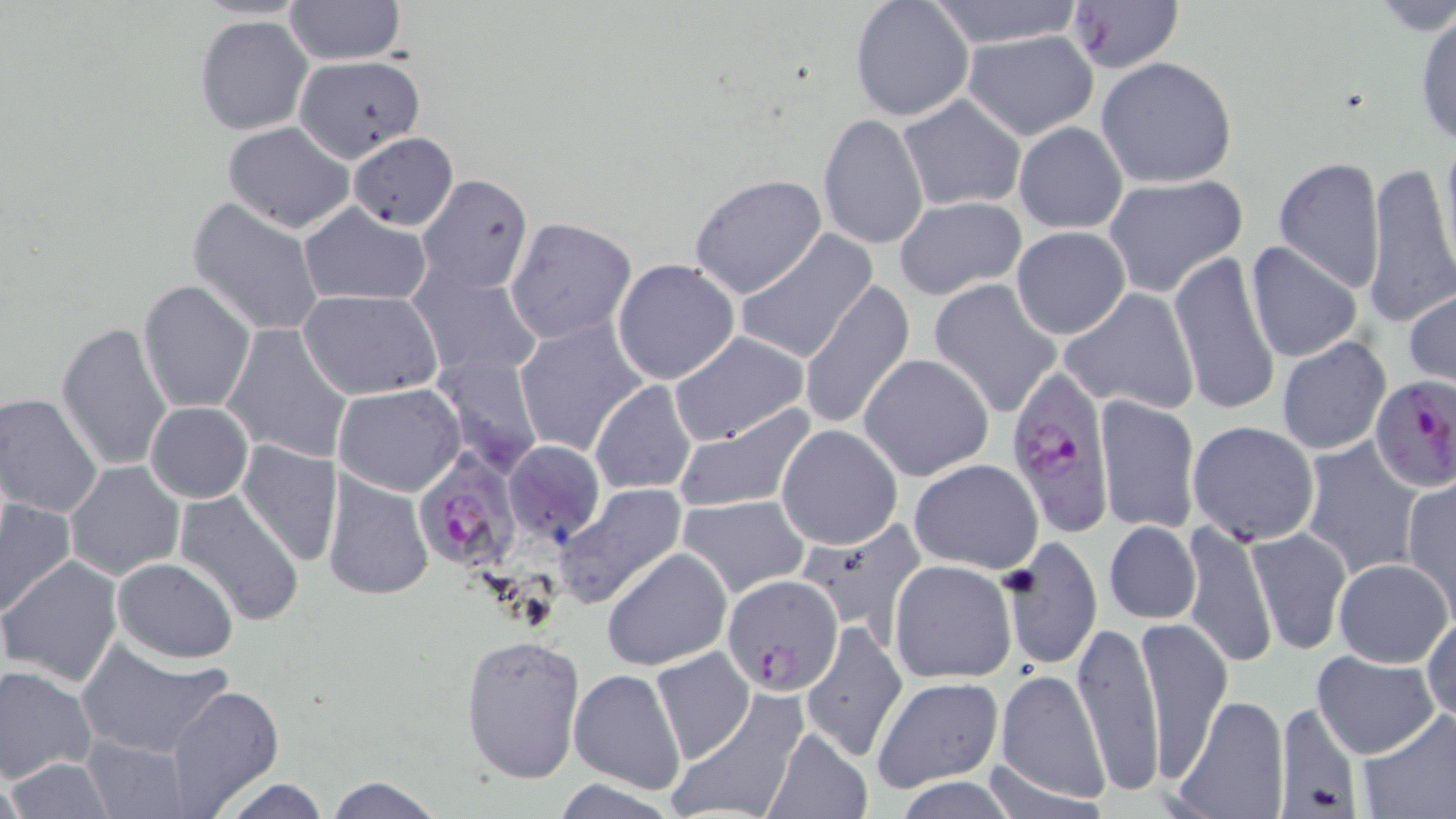
Summary:
  - Coordinate format: approximate bounding boxes as [x1, y1, x2, y2] in pixels
  - Uninfected red blood cell locations: [283, 0, 404, 65], [849, 0, 974, 122], [926, 0, 1083, 49], [1065, 1, 1184, 74], [1412, 9, 1456, 151], [193, 14, 314, 136], [961, 29, 1100, 140], [292, 55, 425, 162], [1097, 56, 1238, 188], [897, 95, 1026, 212], [817, 112, 928, 251], [222, 121, 355, 233], [1014, 121, 1127, 234], [348, 132, 459, 231], [1438, 135, 1456, 270], [1273, 157, 1385, 291], [1362, 162, 1456, 327], [688, 173, 828, 301], [415, 174, 533, 294], [1101, 174, 1247, 296], [895, 195, 1027, 300], [186, 197, 325, 337], [299, 203, 432, 307], [504, 217, 636, 345], [1011, 226, 1131, 340], [733, 231, 877, 364], [1245, 239, 1363, 364], [1027, 242, 1159, 389], [1170, 248, 1281, 419], [612, 258, 741, 386], [409, 265, 543, 382], [928, 277, 1063, 418], [138, 278, 255, 414], [799, 282, 917, 433], [1060, 288, 1199, 415], [299, 289, 444, 399], [1405, 291, 1456, 388], [514, 319, 648, 457], [57, 321, 175, 474], [221, 323, 354, 463], [669, 332, 809, 446], [1277, 336, 1394, 455], [431, 352, 545, 475], [859, 352, 995, 481], [590, 380, 698, 495], [333, 384, 465, 497], [0, 392, 103, 518], [1094, 393, 1201, 536], [145, 402, 252, 503], [673, 403, 820, 515], [1187, 419, 1320, 544], [777, 424, 902, 549], [235, 438, 344, 566], [1302, 438, 1423, 577], [502, 440, 606, 546], [909, 458, 1043, 572], [66, 461, 184, 579], [322, 470, 434, 602], [1401, 478, 1456, 615], [556, 482, 687, 606], [12, 484, 154, 646], [174, 489, 306, 626], [679, 492, 812, 599], [0, 499, 76, 616], [800, 518, 926, 639], [1182, 520, 1276, 668], [1104, 521, 1200, 624], [1247, 526, 1350, 654], [999, 537, 1105, 669], [602, 547, 732, 671], [112, 556, 239, 662], [3, 557, 123, 686], [1333, 558, 1452, 667], [888, 560, 1017, 682], [1421, 608, 1455, 725], [1135, 613, 1231, 783], [1072, 616, 1163, 800], [800, 621, 906, 763], [460, 634, 585, 783], [76, 638, 233, 758], [649, 647, 756, 764], [1312, 649, 1440, 759], [1, 665, 98, 783], [567, 668, 686, 794], [996, 671, 1109, 803], [871, 676, 1006, 792], [165, 684, 286, 817], [665, 691, 808, 819], [1170, 694, 1291, 819], [1275, 699, 1364, 815], [1359, 706, 1455, 816], [763, 727, 872, 819], [82, 735, 191, 818], [4, 759, 118, 817], [324, 774, 444, 818], [889, 776, 1026, 818], [217, 777, 332, 818]
  - Plasmodium falciparum-infected red blood cell locations: [1007, 363, 1118, 534], [1370, 377, 1455, 494], [412, 449, 520, 572], [724, 574, 844, 695]
  - Slide-level diagnosis: Plasmodium falciparum
  - Image size: 1456×819 pixels
  - Field of view: one of a larger specimen
  - Preparation: thin blood film
  - Magnification: 1000x
  - Stain: May-Grünwald-Giemsa
  - Modality: light microscopy